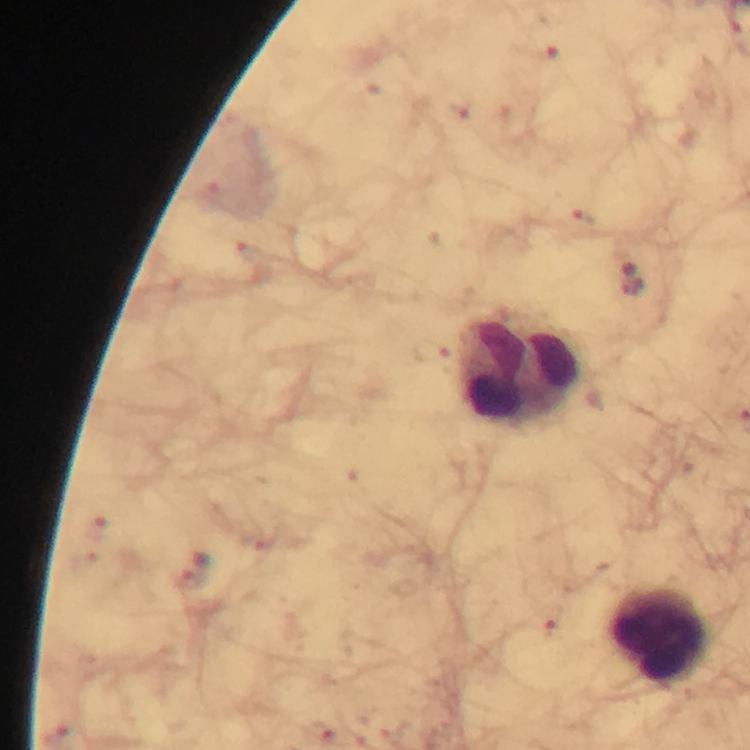
Approximate centers as (x, y) in pixels.
Summary:
  - Leukocyte locations: (519, 368), (660, 635)
  - Malaria parasite locations: (196, 567)
  - Stain: Giemsa
  - Preparation: thick blood smear
  - Capture: smartphone mounted on the microscope
  - Image size: 750×750 pixels
  - Immersion oil: applied
  - Magnification: 100x
  - Context: from a diagnostic examination for malaria
  - Cropped from: one field of view